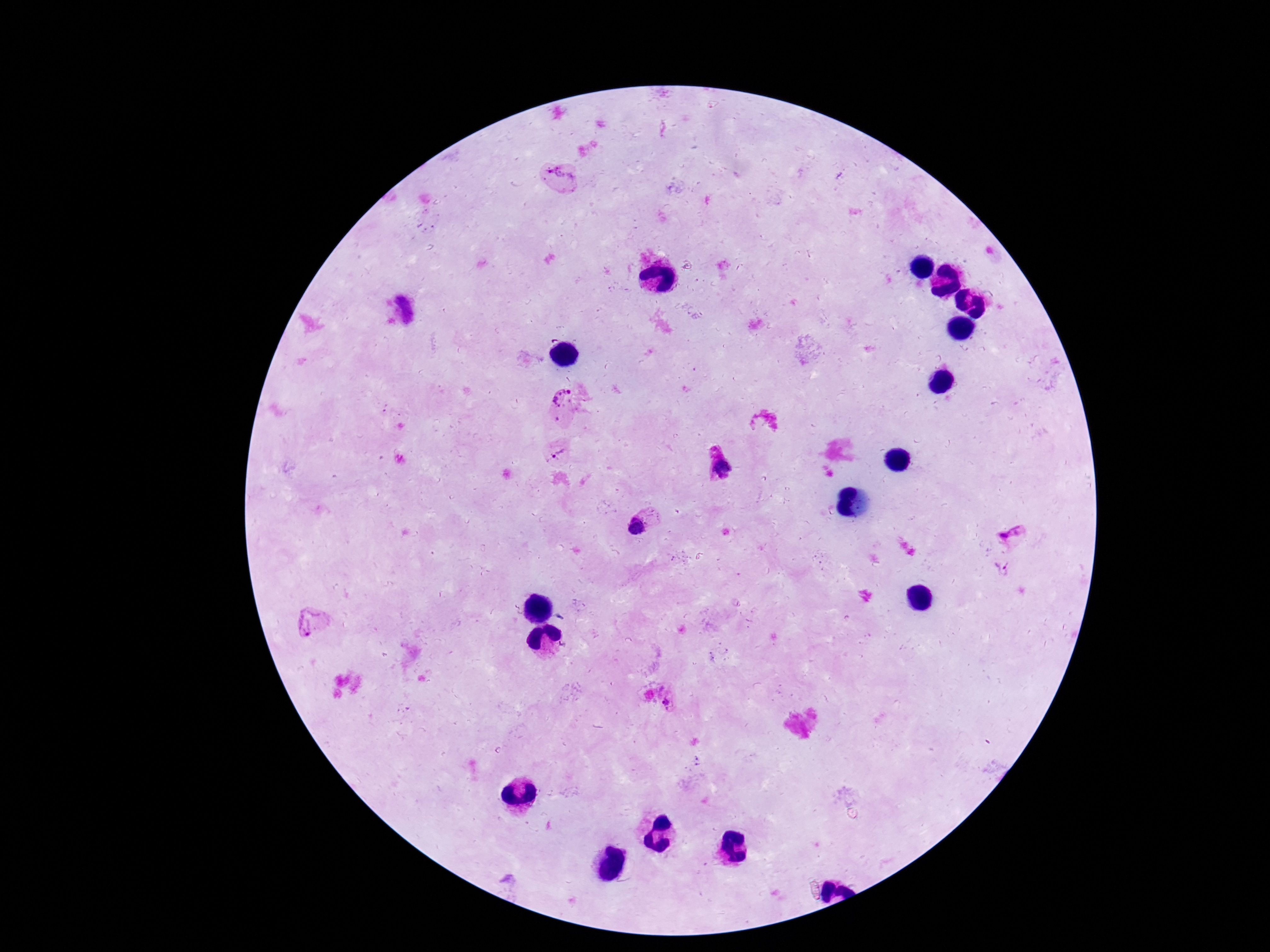
stain = Giemsa
Plasmodium parasite locations = approximate centers as {x, y} in pixels: {562, 182}, {566, 400}, {556, 451}, {721, 468}, {638, 524}, {1009, 531}, {1003, 570}, {310, 624}
preparation = thick peripheral-blood smear
patient malaria status = infected
image size = 1270×952 pixels
capture = smartphone camera through the microscope eyepiece
magnification = 100x
field of view = single